Point out each malaria parasite.
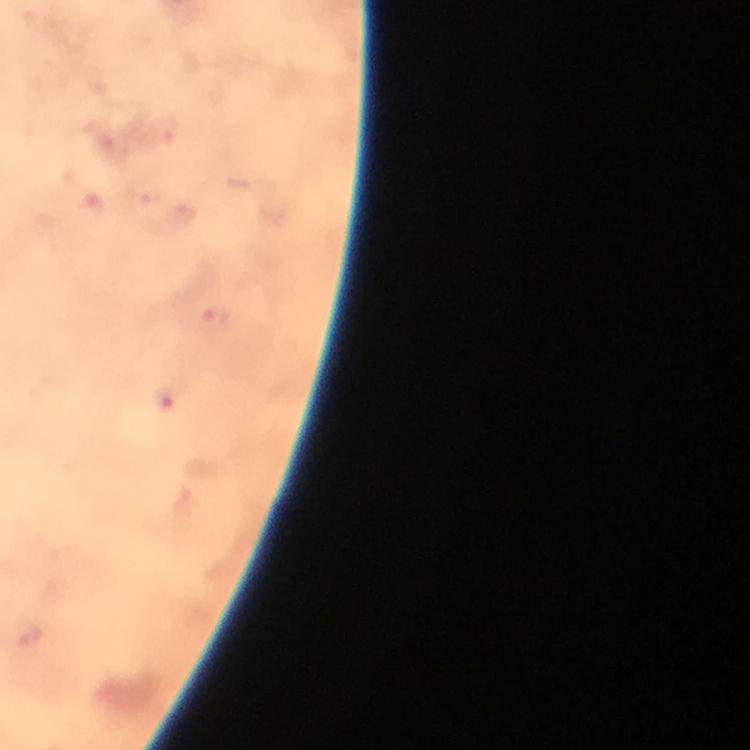
Approximate centers as (x, y) in pixels.
Malaria parasites: (216, 323), (163, 396).

100x magnification. Photographed with a smartphone mounted on the microscope. Image is 750×750 pixels. From a diagnostic examination for malaria. Giemsa-stained preparation. Cropped region of a single field of view. Thick smear. Immersion oil applied.